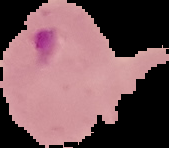
preparation: thin blood film
result: Plasmodium parasites identified
image_type: segmented cell region on a black background
image_size: 169×148 pixels